Identify the parasite.
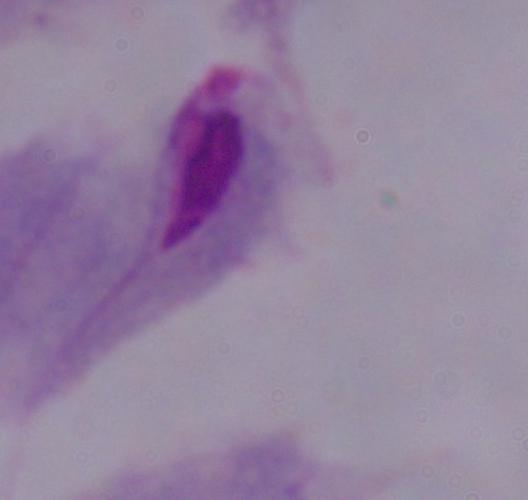

A trichomonad.

1000x magnification. Micrograph.